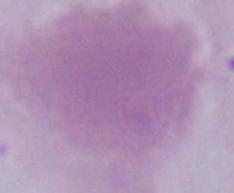

Summary:
  - Magnification: 1000x
  - Identification: erythrocyte
  - Modality: micrograph